Describe the morphology of the erythrocytes.
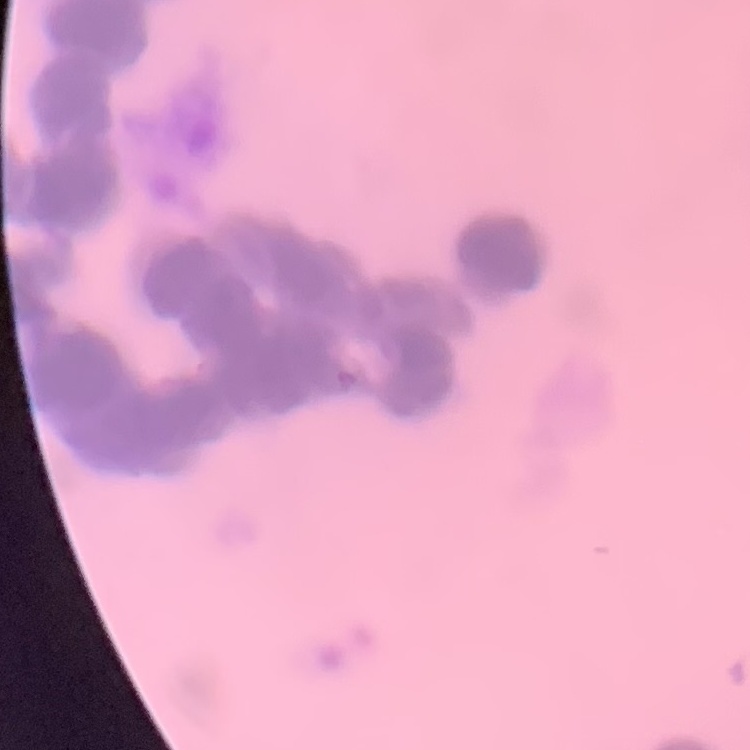
Rouleaux formation.

image type = square crop of a larger photomicrograph
stain = Field's or Giemsa
preparation = thin peripheral smear